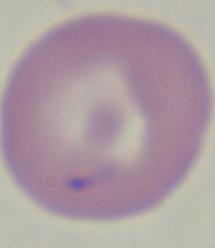

magnification = 1000x
identification = Babesia
modality = micrograph